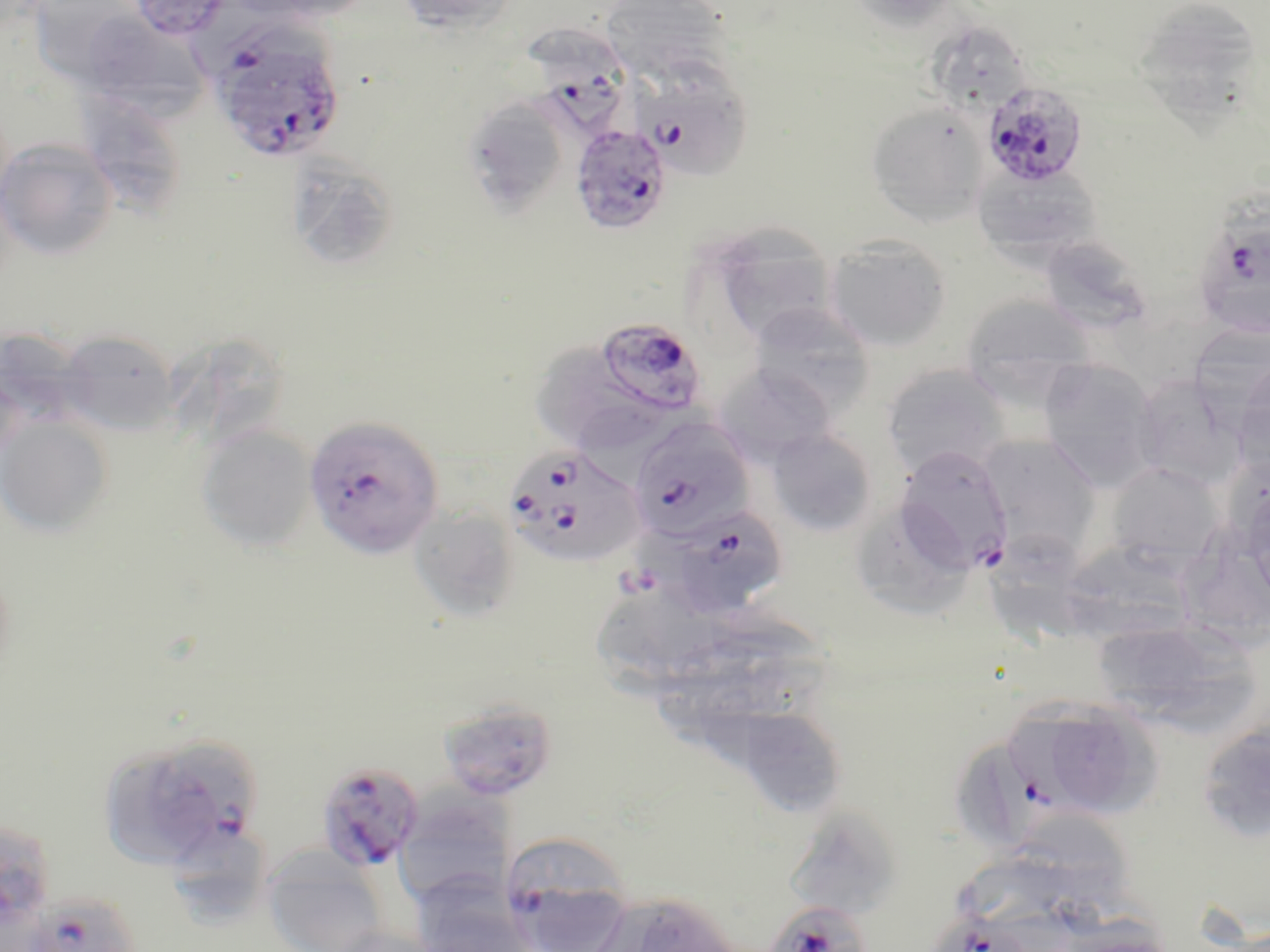

Summary:
  - Coordinate format: approximate bounding boxes as named x1/y1/x2/y2 corners in pixels
  - Uninfected red blood cell locations: (x1=241, y1=0, x2=377, y2=22), (x1=395, y1=0, x2=518, y2=33), (x1=600, y1=0, x2=731, y2=83), (x1=842, y1=0, x2=963, y2=31), (x1=1130, y1=0, x2=1264, y2=120), (x1=28, y1=1, x2=145, y2=86), (x1=90, y1=18, x2=212, y2=122), (x1=925, y1=19, x2=1033, y2=117), (x1=77, y1=90, x2=190, y2=220), (x1=462, y1=96, x2=572, y2=219), (x1=865, y1=100, x2=990, y2=225), (x1=0, y1=137, x2=119, y2=260), (x1=285, y1=153, x2=400, y2=272), (x1=973, y1=164, x2=1102, y2=264), (x1=707, y1=224, x2=839, y2=346), (x1=1039, y1=235, x2=1152, y2=333), (x1=823, y1=236, x2=953, y2=352), (x1=960, y1=293, x2=1096, y2=399), (x1=747, y1=302, x2=876, y2=418), (x1=1190, y1=327, x2=1270, y2=446), (x1=165, y1=329, x2=293, y2=447), (x1=56, y1=331, x2=179, y2=436), (x1=538, y1=336, x2=638, y2=433), (x1=1037, y1=357, x2=1161, y2=488), (x1=714, y1=363, x2=837, y2=466), (x1=881, y1=364, x2=1012, y2=477), (x1=1136, y1=384, x2=1249, y2=486), (x1=577, y1=407, x2=703, y2=487), (x1=0, y1=417, x2=114, y2=536), (x1=196, y1=423, x2=316, y2=552), (x1=766, y1=428, x2=879, y2=536), (x1=976, y1=434, x2=1103, y2=561), (x1=1104, y1=461, x2=1223, y2=568), (x1=856, y1=502, x2=975, y2=618), (x1=408, y1=505, x2=522, y2=624), (x1=1181, y1=520, x2=1270, y2=641), (x1=992, y1=528, x2=1095, y2=644), (x1=1070, y1=544, x2=1200, y2=649), (x1=587, y1=595, x2=716, y2=704), (x1=695, y1=619, x2=829, y2=723), (x1=1091, y1=619, x2=1257, y2=729), (x1=1012, y1=695, x2=1108, y2=801), (x1=437, y1=698, x2=559, y2=804), (x1=1051, y1=702, x2=1164, y2=818), (x1=745, y1=706, x2=847, y2=818), (x1=1195, y1=718, x2=1270, y2=844), (x1=103, y1=747, x2=209, y2=869), (x1=394, y1=790, x2=515, y2=909), (x1=786, y1=802, x2=906, y2=918), (x1=1024, y1=813, x2=1137, y2=916), (x1=0, y1=818, x2=58, y2=933), (x1=174, y1=835, x2=266, y2=921), (x1=261, y1=846, x2=390, y2=952), (x1=947, y1=856, x2=1067, y2=925), (x1=410, y1=875, x2=537, y2=952), (x1=589, y1=891, x2=742, y2=952), (x1=331, y1=923, x2=444, y2=952)
  - Plasmodium falciparum-infected red blood cell locations: (x1=127, y1=1, x2=236, y2=41), (x1=523, y1=24, x2=635, y2=139), (x1=215, y1=33, x2=348, y2=157), (x1=630, y1=58, x2=754, y2=181), (x1=981, y1=81, x2=1088, y2=187), (x1=569, y1=123, x2=673, y2=236), (x1=1193, y1=194, x2=1270, y2=340), (x1=595, y1=316, x2=706, y2=416), (x1=303, y1=414, x2=444, y2=559), (x1=628, y1=418, x2=755, y2=543), (x1=504, y1=443, x2=646, y2=569), (x1=894, y1=445, x2=1013, y2=574), (x1=657, y1=505, x2=789, y2=618), (x1=146, y1=730, x2=263, y2=869), (x1=956, y1=743, x2=1041, y2=844), (x1=316, y1=759, x2=424, y2=874), (x1=504, y1=846, x2=637, y2=952), (x1=23, y1=891, x2=141, y2=952), (x1=763, y1=899, x2=873, y2=952), (x1=932, y1=914, x2=1025, y2=952)
  - Slide-level diagnosis: Plasmodium falciparum
  - Modality: light microscopy
  - Magnification: 1000x
  - Field of view: one of a larger specimen
  - Stain: May-Grünwald-Giemsa
  - Image size: 1270×952 pixels
  - Preparation: thin blood smear